Report the malaria status of this cell.
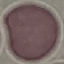

It is uninfected.

stain = Giemsa
image type = cell patch, automatically extracted from a larger field of view and resized to 64 × 64 pixels
capture = smartphone camera at the microscope eyepiece
preparation = thin blood film